Locate and identify every blood parasite.
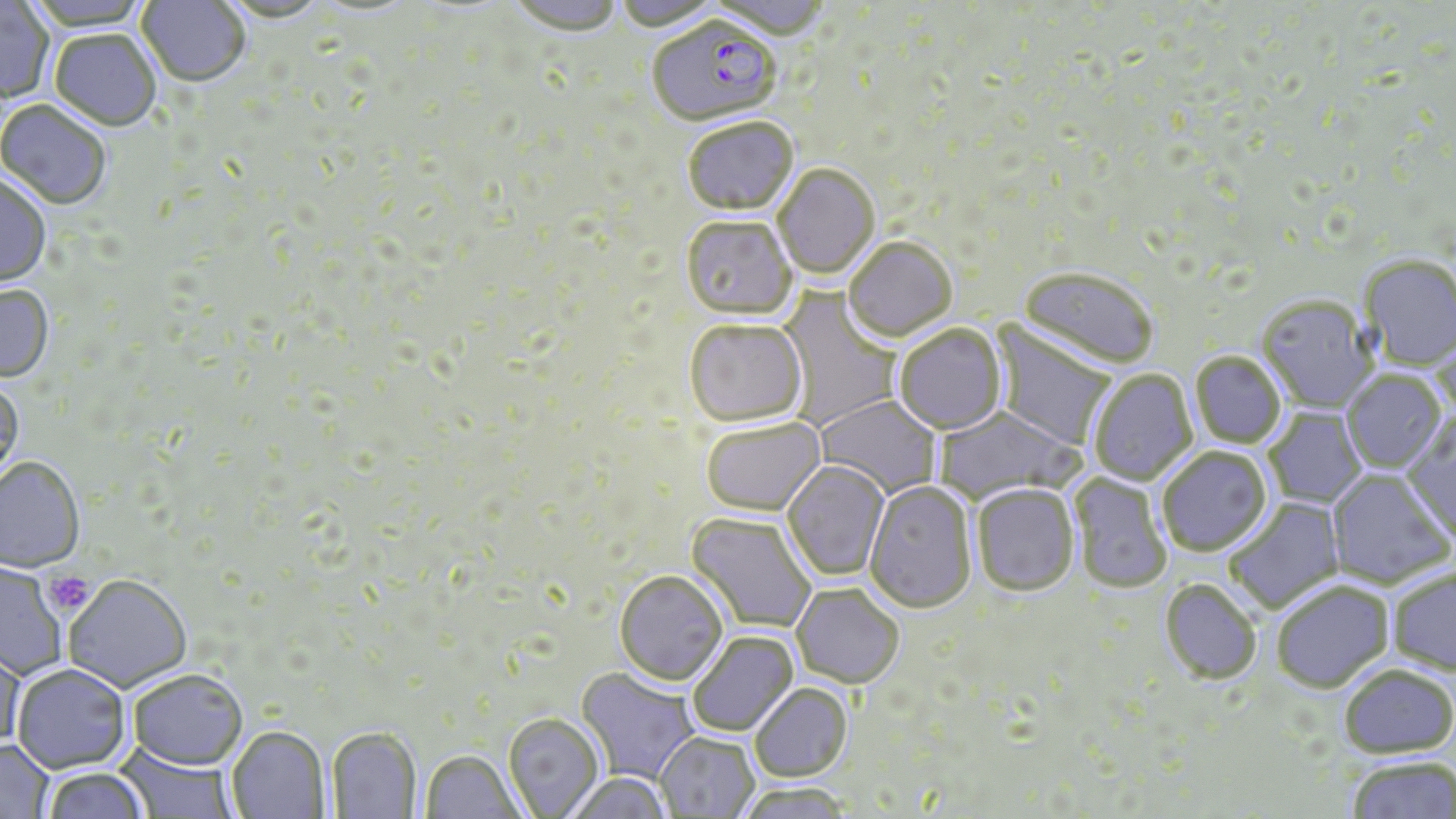

Approximate bounding boxes as named x1/y1/x2/y2 corners in pixels.
Plasmodium falciparum-infected red blood cells: (x1=647, y1=20, x2=782, y2=129).
No Plasmodium ovale, Plasmodium malariae, Plasmodium vivax, Babesia divergens, or Trypanosoma brucei observed.

Summary:
  - Platelet locations: (x1=44, y1=571, x2=94, y2=616)
  - Uninfected red blood cell locations: (x1=26, y1=0, x2=152, y2=33), (x1=136, y1=0, x2=250, y2=90), (x1=220, y1=0, x2=333, y2=26), (x1=506, y1=0, x2=623, y2=38), (x1=613, y1=0, x2=725, y2=34), (x1=708, y1=0, x2=832, y2=42), (x1=0, y1=1, x2=52, y2=104), (x1=50, y1=31, x2=160, y2=133), (x1=0, y1=101, x2=111, y2=211), (x1=683, y1=120, x2=799, y2=219), (x1=774, y1=165, x2=880, y2=281), (x1=0, y1=174, x2=52, y2=289), (x1=680, y1=218, x2=797, y2=323), (x1=844, y1=239, x2=958, y2=345), (x1=1359, y1=256, x2=1456, y2=372), (x1=1017, y1=270, x2=1157, y2=372), (x1=0, y1=286, x2=54, y2=384), (x1=775, y1=288, x2=902, y2=430), (x1=1256, y1=298, x2=1379, y2=415), (x1=684, y1=321, x2=808, y2=430), (x1=989, y1=321, x2=1119, y2=451), (x1=894, y1=326, x2=1007, y2=437), (x1=1431, y1=329, x2=1456, y2=430), (x1=1190, y1=353, x2=1285, y2=449), (x1=1088, y1=370, x2=1198, y2=487), (x1=1341, y1=372, x2=1446, y2=475), (x1=0, y1=379, x2=25, y2=490), (x1=813, y1=395, x2=942, y2=499), (x1=933, y1=406, x2=1083, y2=505), (x1=1264, y1=406, x2=1368, y2=510), (x1=1400, y1=416, x2=1456, y2=544), (x1=701, y1=419, x2=827, y2=519), (x1=1158, y1=448, x2=1272, y2=558), (x1=0, y1=458, x2=85, y2=575), (x1=782, y1=461, x2=890, y2=582), (x1=1326, y1=470, x2=1454, y2=589), (x1=1069, y1=472, x2=1172, y2=595), (x1=863, y1=482, x2=978, y2=616), (x1=971, y1=486, x2=1079, y2=599), (x1=1224, y1=497, x2=1346, y2=615), (x1=685, y1=513, x2=815, y2=634), (x1=0, y1=564, x2=66, y2=679), (x1=1387, y1=567, x2=1456, y2=675), (x1=614, y1=572, x2=729, y2=689), (x1=63, y1=577, x2=192, y2=695), (x1=1159, y1=580, x2=1262, y2=686), (x1=1272, y1=580, x2=1394, y2=693), (x1=791, y1=586, x2=903, y2=690), (x1=687, y1=632, x2=800, y2=738), (x1=0, y1=643, x2=26, y2=752), (x1=1338, y1=664, x2=1456, y2=758), (x1=12, y1=666, x2=132, y2=776), (x1=575, y1=668, x2=700, y2=785), (x1=128, y1=672, x2=248, y2=775), (x1=750, y1=684, x2=853, y2=784), (x1=502, y1=715, x2=604, y2=817), (x1=227, y1=728, x2=330, y2=819), (x1=326, y1=729, x2=422, y2=818), (x1=655, y1=732, x2=758, y2=818), (x1=0, y1=740, x2=54, y2=819), (x1=113, y1=741, x2=240, y2=818), (x1=420, y1=752, x2=524, y2=818), (x1=1346, y1=757, x2=1456, y2=819), (x1=43, y1=769, x2=149, y2=819), (x1=564, y1=775, x2=672, y2=819), (x1=735, y1=785, x2=854, y2=819)
  - Slide-level diagnosis: Plasmodium falciparum
  - Field of view: one of a larger specimen
  - Magnification: 1000x
  - Image size: 1456×819 pixels
  - Modality: light microscopy
  - Stain: May-Grünwald-Giemsa
  - Preparation: thin blood film